Report the malaria status of this cell.
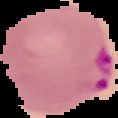

Parasitized.

Image is 118×118 pixels. From a thin blood film. Cell region segmented out of the field of view; the surrounding area is masked to black.